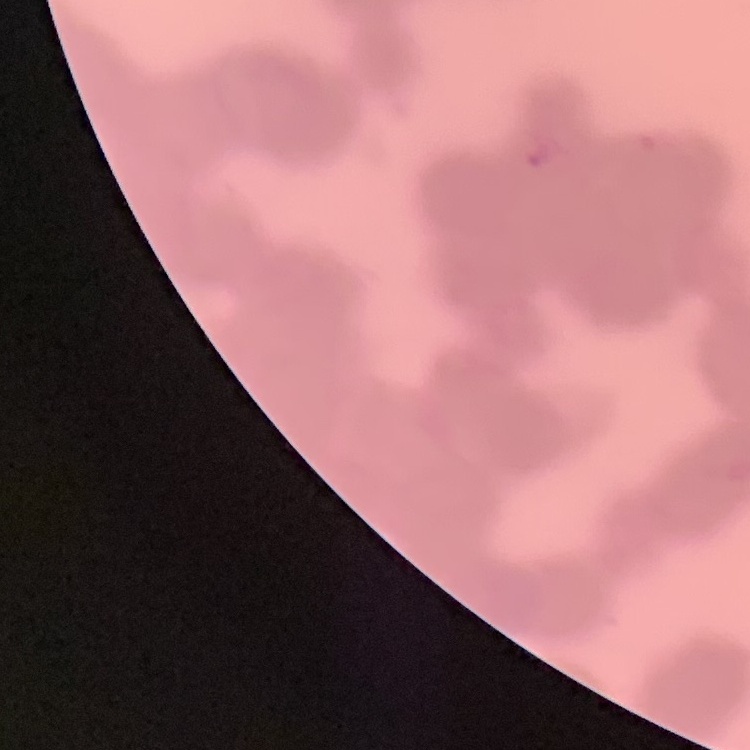

The red blood cells show rouleaux formation. Field's or Giemsa stain. Thin blood smear. One tile cut from a larger photomicrograph.